Report the malaria status of this cell.
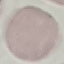
Uninfected.

Summary:
  - Capture: smartphone through the microscope eyepiece
  - Preparation: thin smear
  - Stain: Giemsa
  - Image type: automatically extracted cell patch, resized to 64 × 64 pixels